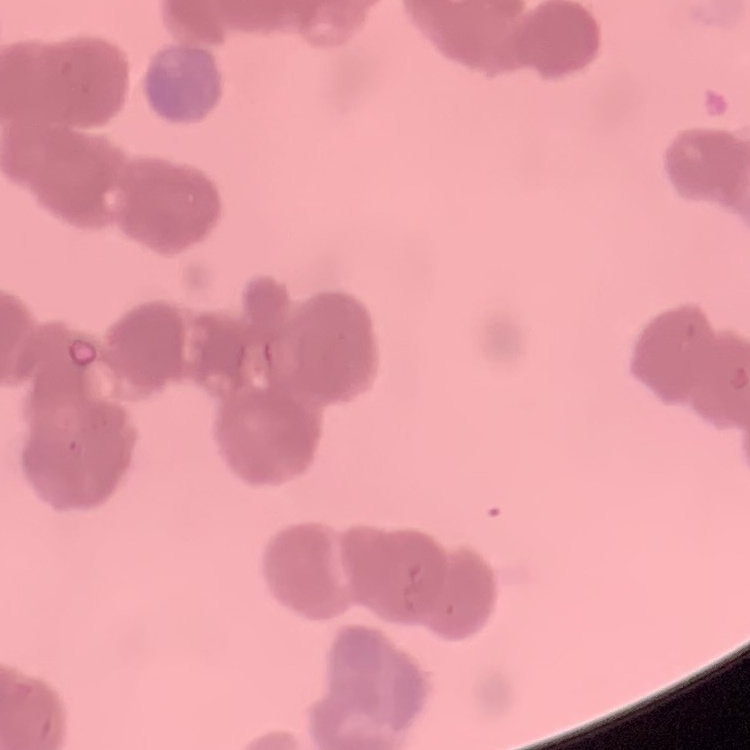

Summary:
  - Erythrocyte morphology: rouleaux formation
  - Preparation: thin blood smear
  - Image type: square crop of a larger photomicrograph
  - Stain: Field's or Giemsa